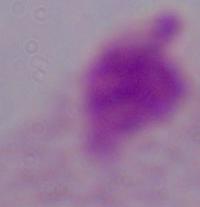 A trichomonad is seen. Micrograph. 1000x magnification.